Name the blood parasite species.
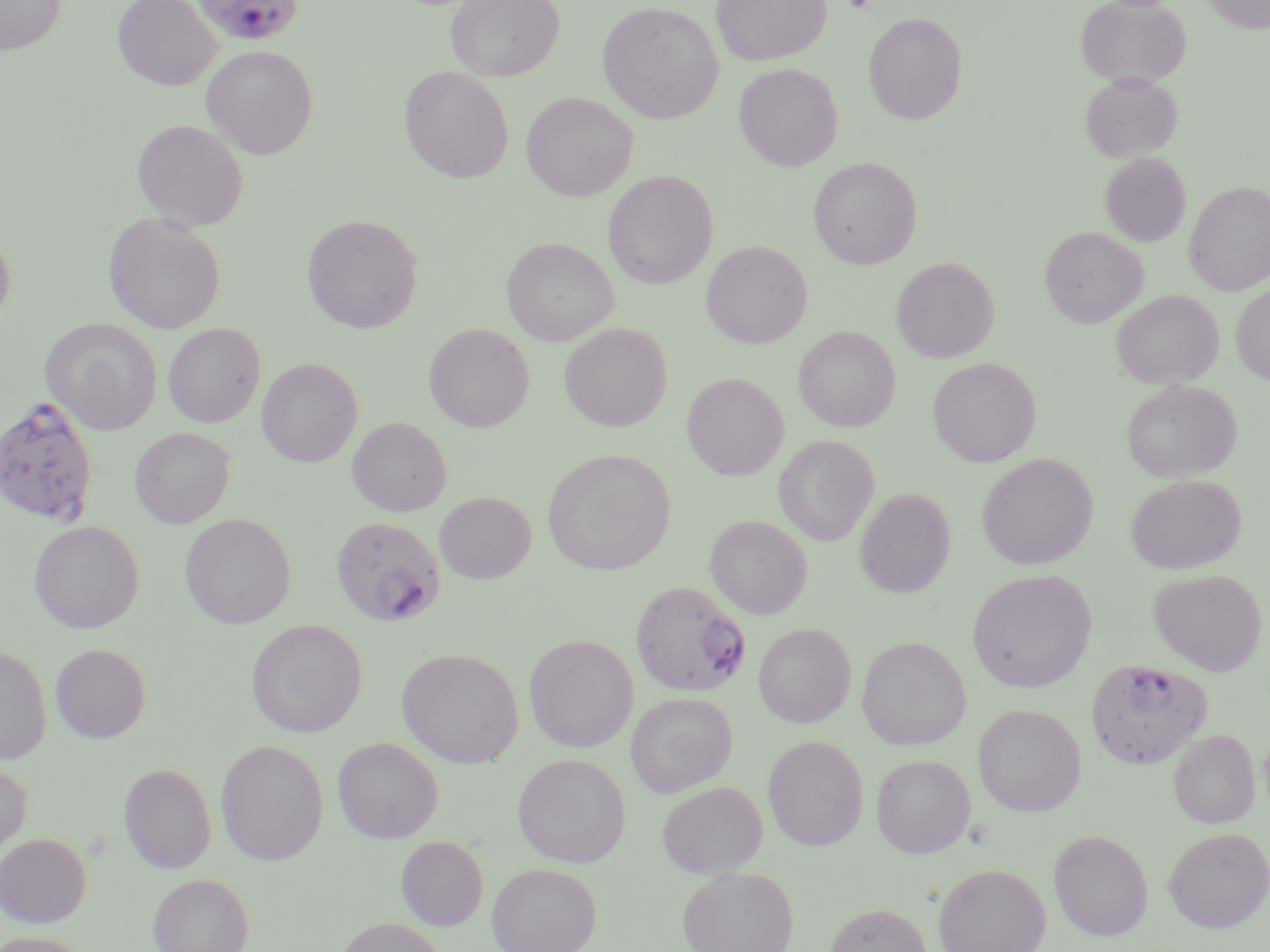

Plasmodium falciparum.

Summary:
  - Coordinate format: approximate bounding boxes as (x1, y1, x2, y2) in pixels
  - Platelet locations: (842, 0, 875, 14)
  - Uninfected red blood cell locations: (0, 0, 67, 55), (113, 0, 221, 90), (445, 0, 564, 81), (711, 0, 831, 65), (1075, 0, 1190, 88), (1201, 0, 1270, 33), (598, 2, 724, 124), (864, 12, 967, 123), (201, 45, 318, 159), (734, 63, 843, 171), (399, 67, 514, 183), (1080, 73, 1182, 162), (522, 92, 638, 201), (132, 119, 249, 230), (1100, 152, 1191, 246), (808, 157, 922, 269), (603, 170, 718, 289), (1185, 181, 1270, 295), (103, 213, 226, 334), (302, 214, 423, 333), (0, 226, 16, 329), (1039, 227, 1147, 327), (502, 237, 618, 345), (701, 240, 812, 348), (892, 257, 999, 362), (1231, 283, 1270, 385), (1112, 290, 1223, 389), (41, 318, 162, 435), (163, 323, 265, 427), (424, 323, 535, 431), (559, 323, 672, 431), (793, 325, 900, 432), (928, 357, 1041, 467), (257, 358, 362, 467), (682, 372, 789, 480), (1121, 379, 1241, 482), (347, 417, 452, 516), (130, 427, 235, 528), (774, 435, 878, 545), (543, 449, 675, 575), (976, 454, 1097, 570), (1125, 474, 1245, 574), (855, 488, 955, 598), (434, 491, 536, 583), (180, 513, 297, 629), (705, 515, 812, 619), (29, 520, 144, 633), (1148, 568, 1267, 676), (967, 569, 1096, 692), (246, 619, 367, 737), (753, 622, 856, 728), (524, 634, 638, 752), (857, 636, 971, 750), (50, 643, 150, 743), (0, 645, 52, 765), (396, 647, 524, 767), (626, 692, 737, 798), (973, 704, 1086, 815), (1169, 728, 1259, 829), (763, 735, 869, 851), (333, 736, 443, 843), (215, 739, 329, 866), (512, 754, 630, 867), (871, 754, 975, 858), (0, 760, 32, 862), (118, 762, 216, 874), (656, 780, 767, 878), (1163, 826, 1269, 932), (1048, 828, 1153, 941), (0, 833, 92, 927), (395, 835, 488, 930), (934, 862, 1051, 952), (487, 863, 601, 952), (678, 865, 798, 952), (148, 872, 254, 952), (824, 901, 933, 952), (333, 917, 448, 952), (0, 931, 95, 952)
  - Plasmodium falciparum-infected red blood cell locations: (192, 0, 304, 46), (0, 396, 100, 526), (330, 517, 446, 627), (631, 580, 750, 697), (1086, 659, 1212, 769)
  - Modality: light microscopy
  - Magnification: 1000x
  - Stain: May-Grünwald-Giemsa
  - Image size: 1270×952 pixels
  - Field of view: single
  - Preparation: thin blood smear